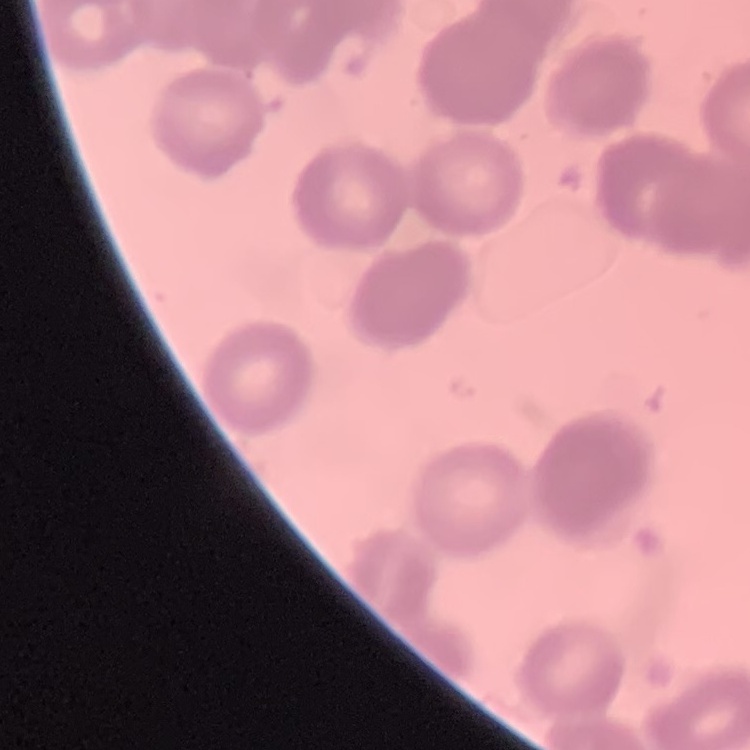

red blood cell morphology = rouleaux formation
preparation = thin blood film
image type = square crop of a larger photomicrograph
stain = Field's or Giemsa